Give the preparation type.
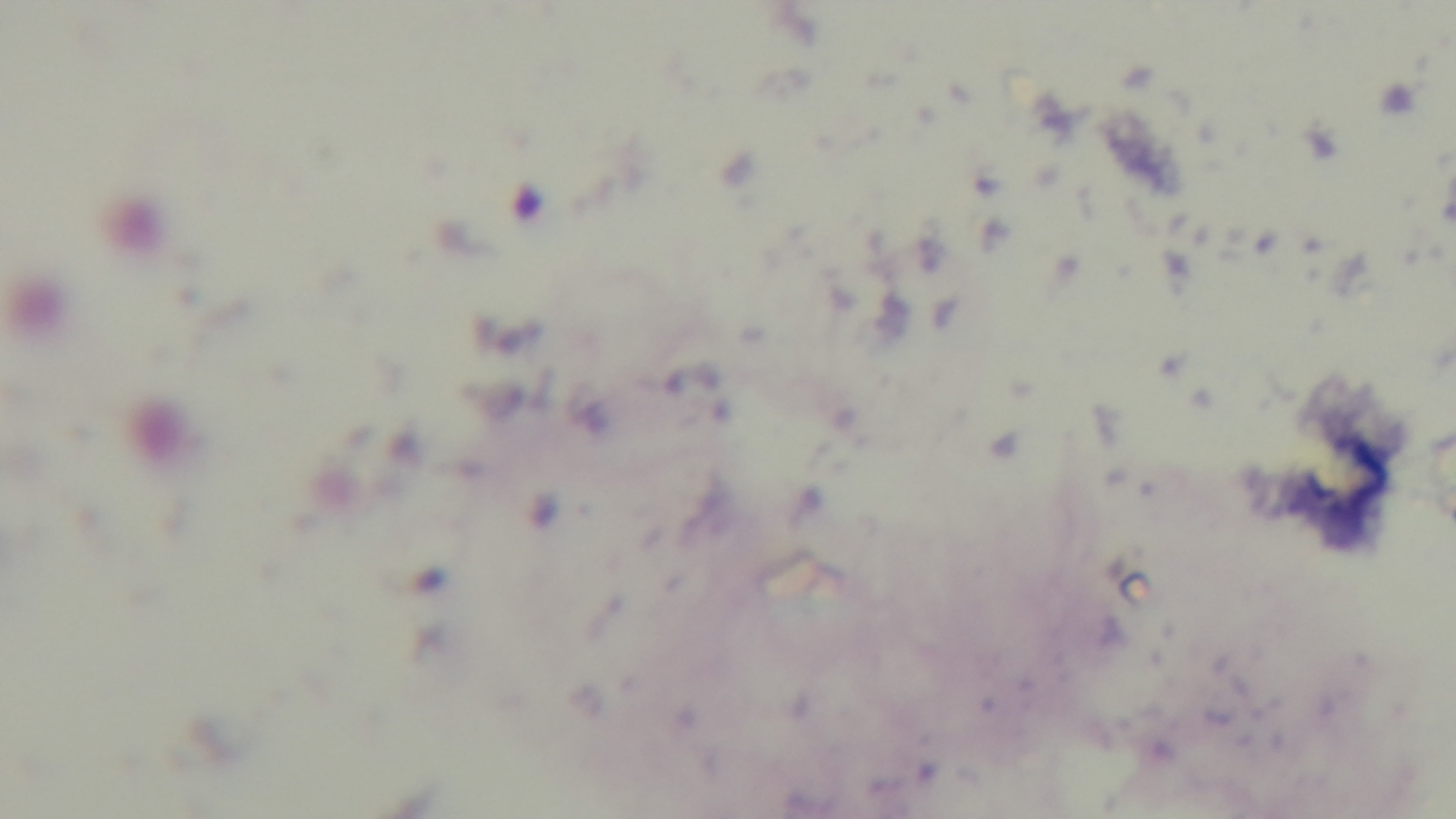

It is a thick blood film.

100x oil-immersion objective. Malaria status: negative. Giemsa-stained. Single field of view. Light microscopy. Captured with a mounted 4K digital camera.